Outline each Plasmodium vivax-infected red blood cell.
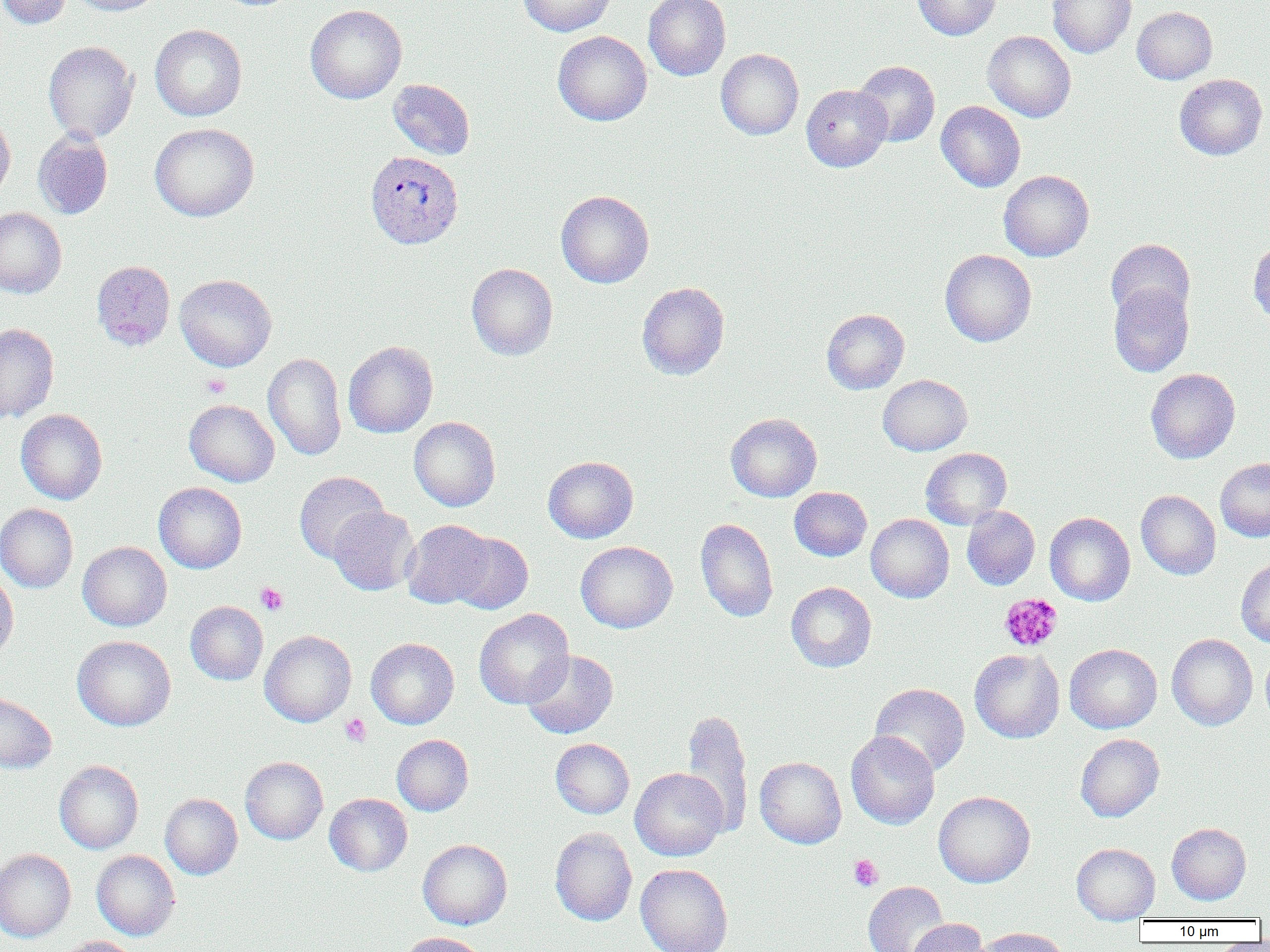

Approximate bounding boxes as named x1/y1/x2/y2 corners in pixels.
Plasmodium vivax-infected red blood cells: (x1=366, y1=151, x2=463, y2=249).

Summary:
  - Platelet locations: (x1=201, y1=373, x2=230, y2=398), (x1=256, y1=582, x2=288, y2=615), (x1=1000, y1=593, x2=1062, y2=652), (x1=340, y1=713, x2=371, y2=747), (x1=849, y1=855, x2=883, y2=891)
  - Uninfected red blood cell locations: (x1=0, y1=0, x2=72, y2=29), (x1=69, y1=0, x2=167, y2=15), (x1=519, y1=0, x2=616, y2=36), (x1=643, y1=0, x2=731, y2=81), (x1=912, y1=0, x2=1000, y2=40), (x1=1047, y1=0, x2=1136, y2=58), (x1=305, y1=4, x2=407, y2=104), (x1=1132, y1=6, x2=1217, y2=84), (x1=150, y1=24, x2=247, y2=121), (x1=553, y1=31, x2=652, y2=125), (x1=982, y1=31, x2=1076, y2=122), (x1=43, y1=41, x2=139, y2=143), (x1=716, y1=48, x2=804, y2=140), (x1=854, y1=61, x2=940, y2=147), (x1=1174, y1=74, x2=1268, y2=160), (x1=388, y1=79, x2=475, y2=160), (x1=801, y1=84, x2=892, y2=171), (x1=935, y1=101, x2=1025, y2=192), (x1=0, y1=111, x2=15, y2=202), (x1=149, y1=123, x2=259, y2=221), (x1=33, y1=130, x2=113, y2=219), (x1=998, y1=170, x2=1094, y2=261), (x1=555, y1=190, x2=654, y2=288), (x1=0, y1=207, x2=67, y2=298), (x1=1106, y1=238, x2=1195, y2=324), (x1=1248, y1=239, x2=1270, y2=326), (x1=940, y1=249, x2=1036, y2=347), (x1=91, y1=260, x2=176, y2=350), (x1=466, y1=263, x2=558, y2=360), (x1=175, y1=274, x2=277, y2=371), (x1=637, y1=281, x2=729, y2=380), (x1=1108, y1=283, x2=1193, y2=377), (x1=822, y1=309, x2=909, y2=394), (x1=0, y1=323, x2=59, y2=423), (x1=343, y1=341, x2=438, y2=438), (x1=263, y1=352, x2=347, y2=460), (x1=1145, y1=368, x2=1240, y2=463), (x1=877, y1=374, x2=972, y2=456), (x1=184, y1=399, x2=279, y2=487), (x1=16, y1=408, x2=107, y2=505), (x1=726, y1=413, x2=822, y2=502), (x1=409, y1=416, x2=500, y2=511), (x1=921, y1=448, x2=1012, y2=528), (x1=543, y1=456, x2=638, y2=543), (x1=1216, y1=458, x2=1270, y2=542), (x1=294, y1=471, x2=388, y2=563), (x1=154, y1=482, x2=247, y2=573), (x1=789, y1=487, x2=872, y2=561), (x1=1136, y1=490, x2=1221, y2=579), (x1=0, y1=503, x2=78, y2=593), (x1=328, y1=505, x2=420, y2=596), (x1=962, y1=506, x2=1040, y2=590), (x1=1045, y1=512, x2=1135, y2=605), (x1=866, y1=514, x2=954, y2=602), (x1=695, y1=517, x2=778, y2=622), (x1=402, y1=519, x2=495, y2=609), (x1=447, y1=531, x2=533, y2=614), (x1=77, y1=541, x2=172, y2=631), (x1=576, y1=541, x2=677, y2=633), (x1=1236, y1=559, x2=1270, y2=647), (x1=0, y1=570, x2=18, y2=663), (x1=786, y1=582, x2=877, y2=672), (x1=185, y1=601, x2=268, y2=685), (x1=473, y1=608, x2=575, y2=709), (x1=259, y1=630, x2=356, y2=727), (x1=1167, y1=634, x2=1257, y2=730), (x1=72, y1=635, x2=176, y2=731), (x1=365, y1=637, x2=459, y2=729), (x1=1064, y1=644, x2=1162, y2=733), (x1=1261, y1=647, x2=1270, y2=725), (x1=969, y1=649, x2=1065, y2=743), (x1=522, y1=650, x2=618, y2=739), (x1=870, y1=683, x2=970, y2=776), (x1=0, y1=692, x2=57, y2=773), (x1=681, y1=709, x2=754, y2=837), (x1=845, y1=730, x2=940, y2=830), (x1=1076, y1=733, x2=1164, y2=822), (x1=392, y1=734, x2=474, y2=816), (x1=550, y1=738, x2=634, y2=818), (x1=240, y1=756, x2=328, y2=844), (x1=755, y1=757, x2=846, y2=848), (x1=54, y1=760, x2=144, y2=854), (x1=630, y1=768, x2=728, y2=861), (x1=933, y1=791, x2=1035, y2=887), (x1=160, y1=793, x2=243, y2=879), (x1=325, y1=793, x2=412, y2=876), (x1=1167, y1=823, x2=1251, y2=904), (x1=550, y1=827, x2=637, y2=926), (x1=418, y1=839, x2=512, y2=929), (x1=1072, y1=843, x2=1160, y2=923), (x1=0, y1=849, x2=75, y2=942), (x1=91, y1=849, x2=180, y2=940), (x1=635, y1=863, x2=733, y2=952), (x1=863, y1=881, x2=951, y2=952), (x1=905, y1=919, x2=988, y2=952), (x1=974, y1=927, x2=1071, y2=952), (x1=396, y1=932, x2=488, y2=952), (x1=55, y1=935, x2=141, y2=952)
  - Slide-level diagnosis: Plasmodium vivax
  - Field of view: one of a larger specimen
  - Magnification: 1000x
  - Preparation: thin blood film
  - Image size: 1270×952 pixels
  - Modality: light microscopy